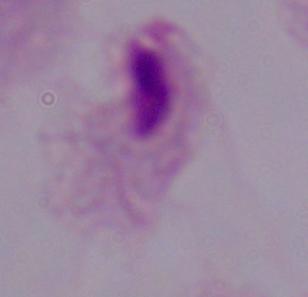
Summary:
  - Modality: micrograph
  - Identification: trichomonad
  - Magnification: 1000x